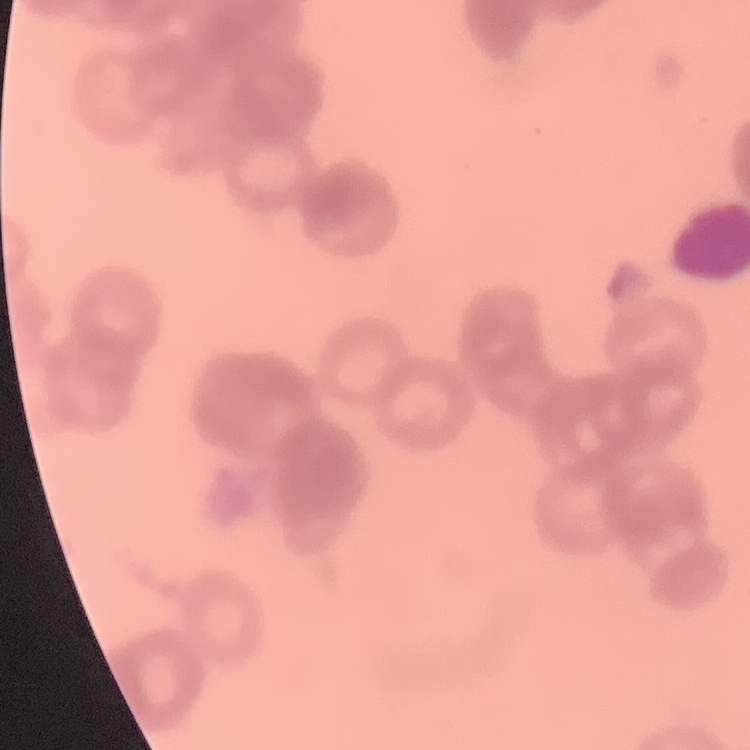

Summary:
  - Red blood cell morphology: rouleaux formation
  - Image type: square crop of a larger photomicrograph
  - Preparation: thin blood film
  - Stain: Field's or Giemsa